Assess this cell for malaria.
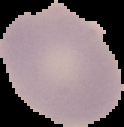
Uninfected.

Image is 124×127 pixels. From a thin blood smear. Segmented cell region on a black background.